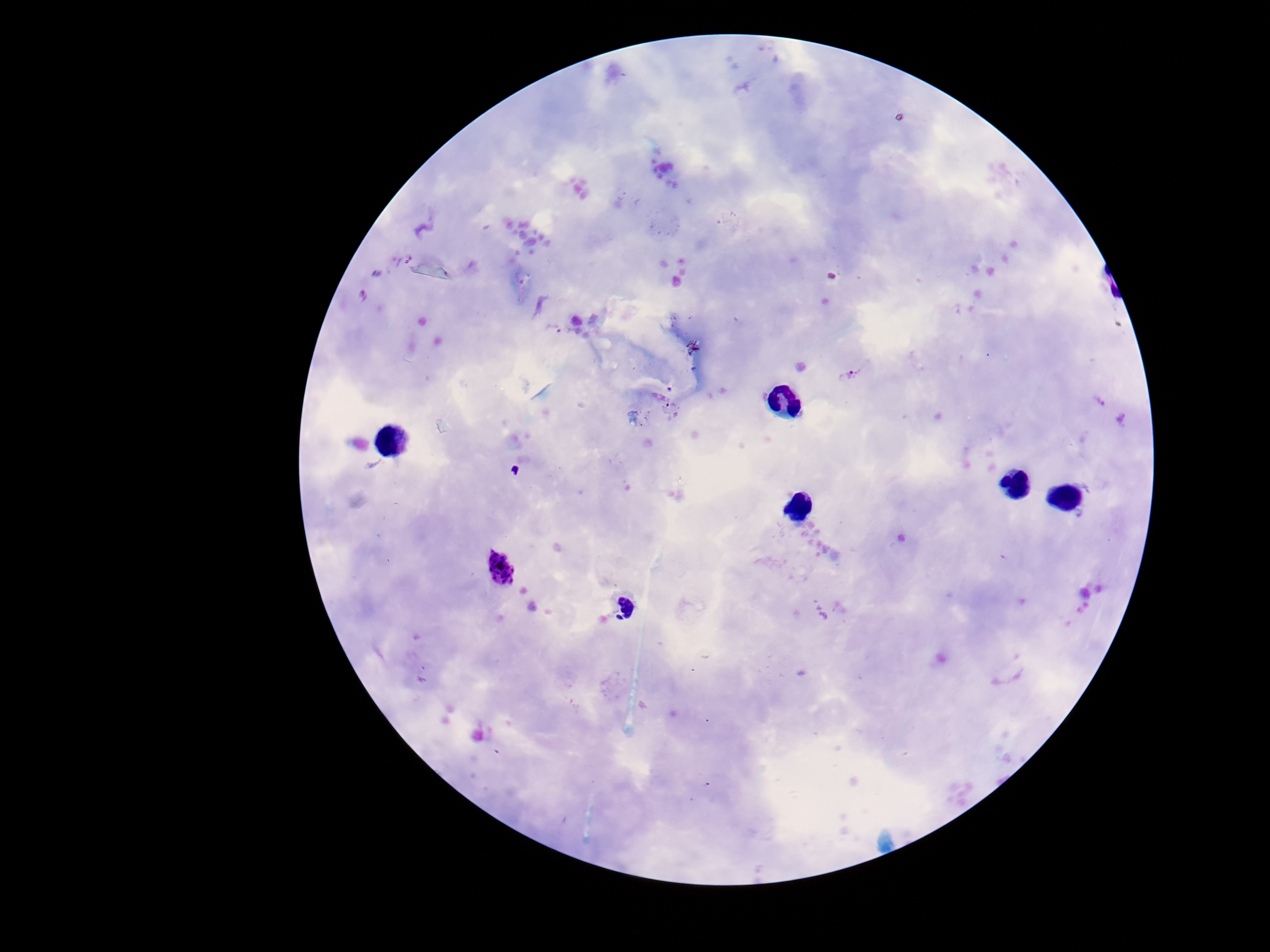

stain: Giemsa
magnification: 100x
patient_malaria_status: infected
preparation: thick blood smear
plasmodium_parasite_locations: 'approximate object centers, in pixels from the top-left corner: (x=853, y=373), (x=503, y=568), (x=621, y=609)'
capture: smartphone camera through the microscope eyepiece
field_of_view: one from this slide
image_size: 1270×952 pixels